State which parasite is depicted.
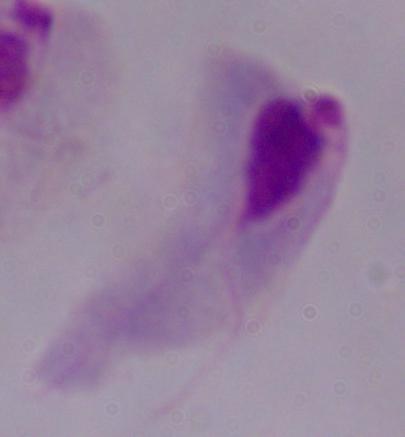

This is a trichomonad.

Summary:
  - Magnification: 1000x
  - Modality: micrograph